Draw a bounding box around every malaria parasite, every leukocyte, and every artifact (stain precipitate or debris).
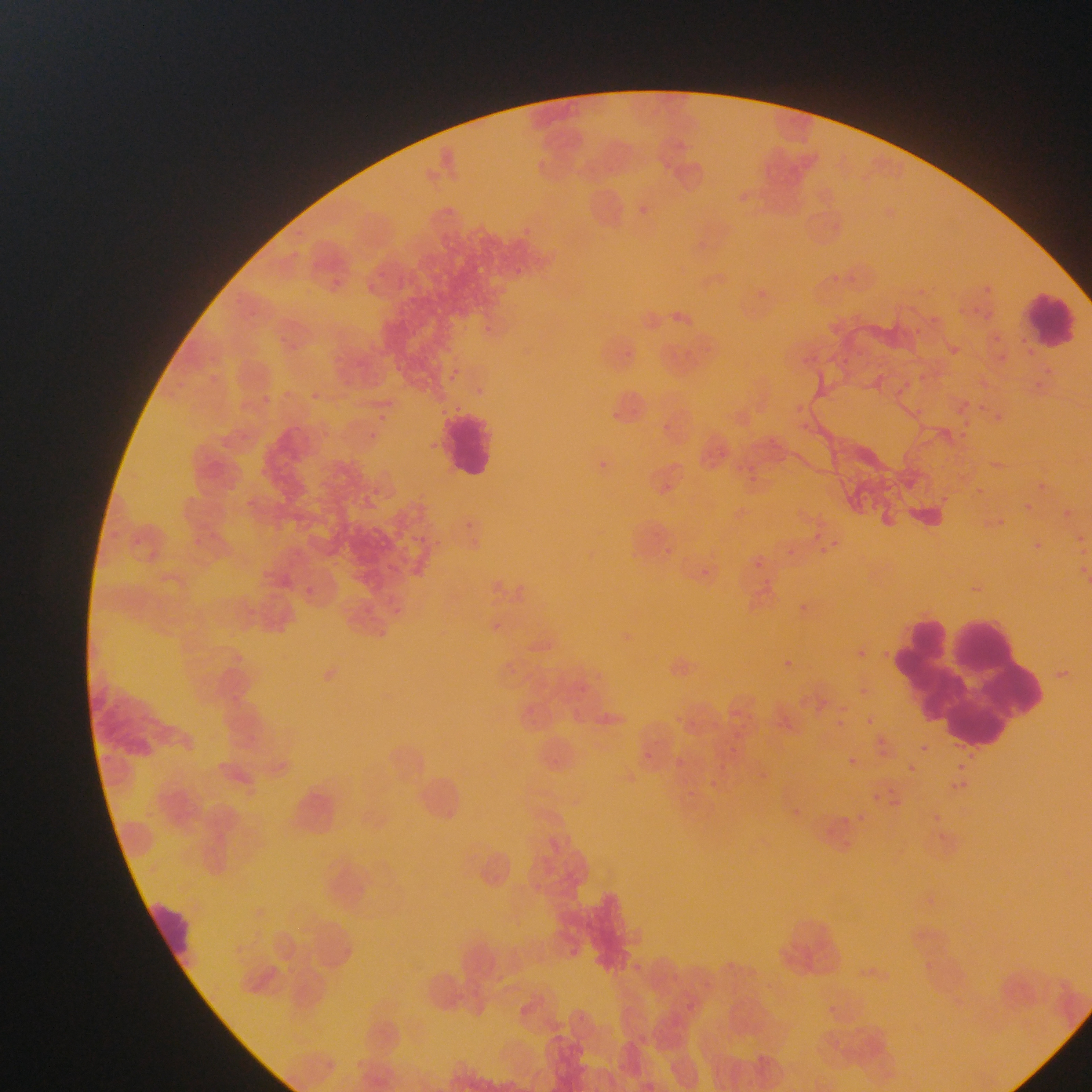

Approximate bounding boxes as {left, top, right, bottom} in pixels.
Malaria parasites: {636, 204, 656, 221}, {518, 225, 548, 246}, {514, 263, 523, 278}, {323, 275, 345, 299}, {983, 282, 1000, 298}, {751, 287, 776, 311}, {980, 308, 996, 327}, {241, 309, 256, 329}, {672, 310, 685, 324}, {488, 321, 508, 335}, {277, 333, 292, 352}, {995, 349, 1008, 365}, {204, 351, 219, 372}, {446, 366, 474, 389}, {207, 373, 223, 392}, {903, 373, 916, 382}, {342, 379, 353, 395}, {281, 387, 294, 400}, {256, 391, 269, 404}, {312, 391, 325, 411}, {794, 396, 814, 415}, {954, 399, 988, 436}, {913, 403, 928, 417}, {608, 409, 624, 427}, {375, 410, 389, 423}, {363, 431, 379, 443}, {708, 443, 730, 462}, {595, 453, 611, 467}, {997, 457, 1011, 473}, {741, 462, 763, 487}, {1036, 478, 1048, 488}, {958, 485, 995, 507}, {1023, 500, 1033, 513}, {1066, 508, 1078, 520}, {813, 527, 824, 537}, {1075, 532, 1092, 551}, {830, 535, 846, 549}, {429, 540, 454, 555}, {1036, 540, 1052, 560}, {660, 543, 676, 559}, {815, 543, 828, 556}, {751, 552, 768, 572}, {702, 557, 711, 573}, {1080, 559, 1092, 580}, {301, 583, 320, 596}, {794, 601, 807, 609}, {395, 603, 405, 616}, {486, 619, 502, 638}, {849, 642, 868, 667}, {785, 655, 796, 668}, {860, 681, 874, 694}, {606, 708, 623, 734}, {865, 710, 875, 722}, {818, 714, 840, 729}, {723, 743, 742, 759}, {920, 744, 929, 753}, {641, 747, 654, 768}, {678, 751, 691, 771}, {848, 758, 856, 765}, {908, 764, 917, 772}, {957, 765, 965, 772}, {706, 776, 722, 791}, {953, 780, 967, 797}, {868, 781, 907, 808}, {682, 790, 705, 808}, {933, 803, 946, 828}, {836, 813, 856, 836}, {529, 877, 551, 908}, {567, 941, 578, 954}, {537, 952, 554, 969}, {927, 956, 945, 970}, {494, 969, 512, 989}, {681, 1001, 698, 1017}.
Leukocytes: {1026, 285, 1081, 353}, {440, 405, 500, 483}, {892, 604, 1068, 731}, {151, 898, 192, 976}.

{
  "preparation": "thin blood smear",
  "country": "Ghana",
  "image_size": "1092×1092 pixels",
  "capture": "mobile-phone photograph through a microscope",
  "field_of_view": "single"
}